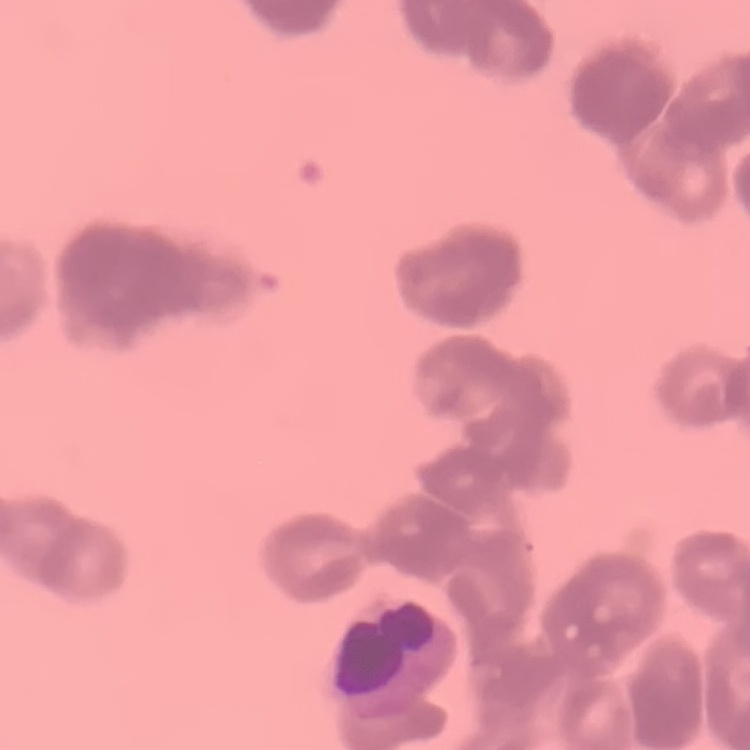

The erythrocytes exhibit rouleaux formation. Thin peripheral smear. Square crop of a larger photomicrograph. Stained with either Field's or Giemsa.